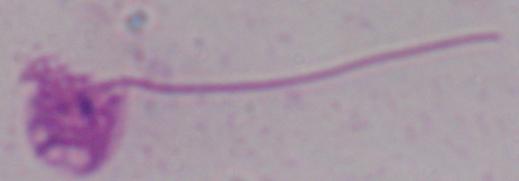
modality = photomicrograph
identification = Leishmania
magnification = 1000x